Identify the cell.
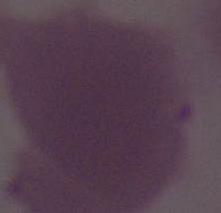

This is an erythrocyte.

{
  "magnification": "1000x",
  "modality": "micrograph"
}